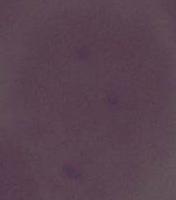

Summary:
  - Identification: red blood cell
  - Modality: micrograph
  - Magnification: 1000x